Identify the cell.
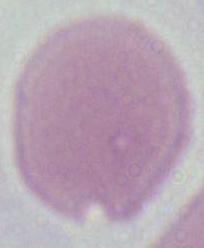

This is an erythrocyte.

Captured at 1000x magnification. Photomicrograph.